Outline each blood parasite and name the species.
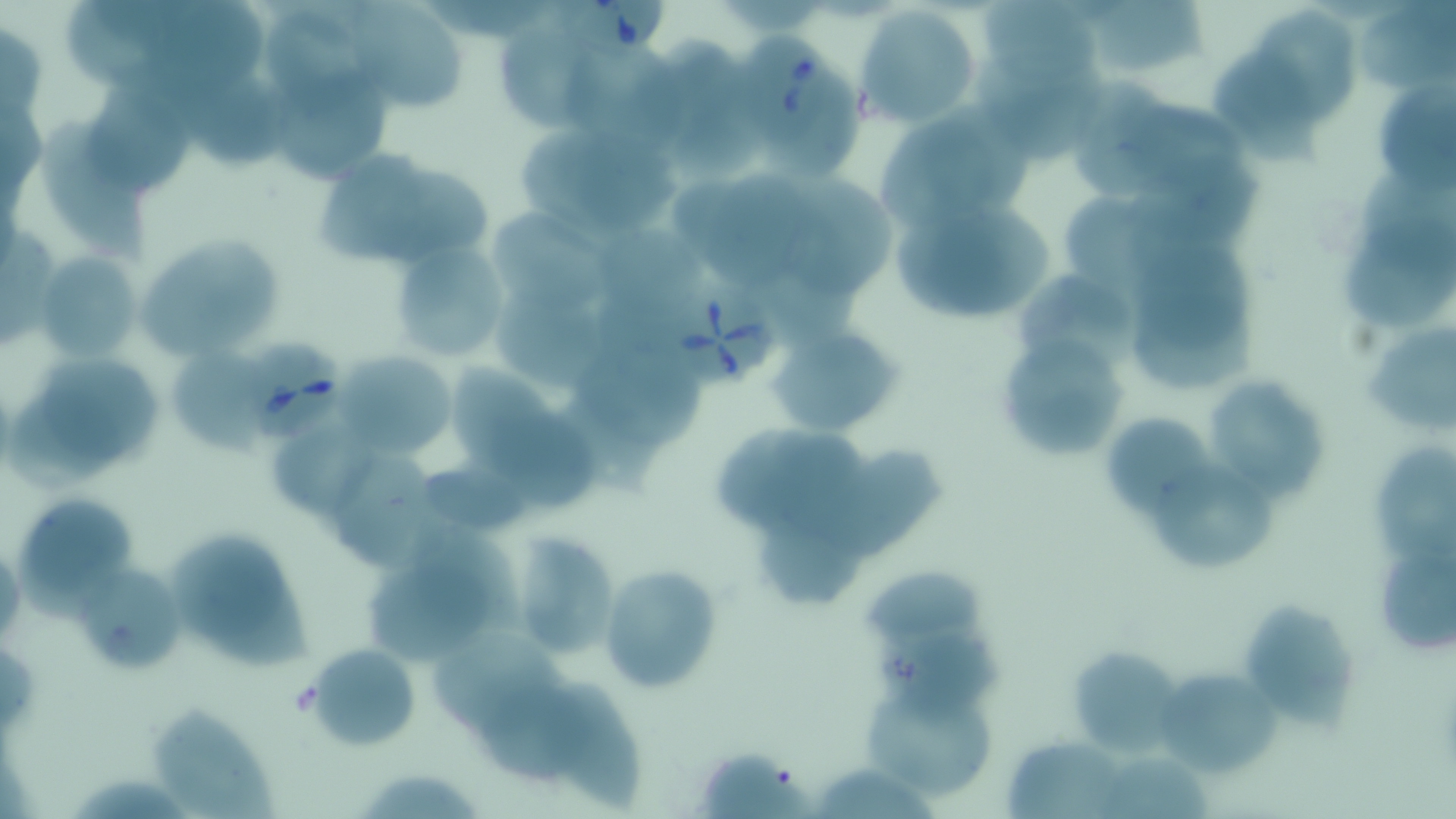

Approximate bounding boxes as named x1/y1/x2/y2 corners in pixels.
Babesia divergens-infected red blood cells: (x1=552, y1=1, x2=667, y2=58), (x1=731, y1=18, x2=832, y2=138), (x1=664, y1=282, x2=774, y2=386), (x1=235, y1=341, x2=348, y2=443).
No Plasmodium falciparum, Plasmodium ovale, Plasmodium malariae, Plasmodium vivax, or Trypanosoma brucei observed.

{
  "slide_level_diagnosis": "Babesia divergens",
  "field_of_view": "single",
  "uninfected_red_blood_cell_locations": "approximate bounding boxes as named x1/y1/x2/y2 corners in pixels: (x1=63, y1=0, x2=170, y2=87), (x1=986, y1=0, x2=1102, y2=85), (x1=1093, y1=0, x2=1212, y2=71), (x1=1358, y1=0, x2=1456, y2=96), (x1=359, y1=3, x2=467, y2=114), (x1=156, y1=4, x2=270, y2=90), (x1=856, y1=4, x2=984, y2=127), (x1=1259, y1=8, x2=1358, y2=123), (x1=262, y1=10, x2=367, y2=89), (x1=498, y1=19, x2=601, y2=127), (x1=653, y1=34, x2=745, y2=122), (x1=563, y1=37, x2=677, y2=153), (x1=978, y1=44, x2=1106, y2=166), (x1=1215, y1=49, x2=1325, y2=175), (x1=266, y1=63, x2=393, y2=183), (x1=179, y1=68, x2=288, y2=171), (x1=768, y1=71, x2=854, y2=177), (x1=1078, y1=77, x2=1175, y2=199), (x1=1374, y1=82, x2=1456, y2=201), (x1=82, y1=86, x2=195, y2=190), (x1=674, y1=98, x2=764, y2=181), (x1=1118, y1=99, x2=1249, y2=195), (x1=880, y1=115, x2=997, y2=229), (x1=41, y1=118, x2=149, y2=265), (x1=517, y1=123, x2=680, y2=249), (x1=318, y1=144, x2=421, y2=266), (x1=1141, y1=157, x2=1274, y2=241), (x1=388, y1=167, x2=502, y2=269), (x1=702, y1=171, x2=826, y2=288), (x1=793, y1=177, x2=899, y2=298), (x1=1360, y1=178, x2=1456, y2=280), (x1=894, y1=194, x2=1059, y2=328), (x1=1063, y1=197, x2=1176, y2=286), (x1=490, y1=204, x2=611, y2=320), (x1=600, y1=229, x2=714, y2=309), (x1=136, y1=234, x2=285, y2=357), (x1=1135, y1=235, x2=1253, y2=357), (x1=1341, y1=236, x2=1454, y2=322), (x1=387, y1=238, x2=512, y2=364), (x1=38, y1=252, x2=144, y2=367), (x1=757, y1=264, x2=859, y2=349), (x1=1016, y1=275, x2=1143, y2=371), (x1=595, y1=282, x2=694, y2=365), (x1=489, y1=294, x2=614, y2=386), (x1=1364, y1=318, x2=1456, y2=434), (x1=767, y1=324, x2=901, y2=438), (x1=995, y1=340, x2=1126, y2=463), (x1=583, y1=345, x2=706, y2=450), (x1=33, y1=350, x2=163, y2=465), (x1=335, y1=352, x2=456, y2=460), (x1=452, y1=359, x2=562, y2=466), (x1=1204, y1=377, x2=1327, y2=500), (x1=558, y1=388, x2=667, y2=495), (x1=1109, y1=406, x2=1208, y2=514), (x1=262, y1=408, x2=373, y2=523), (x1=490, y1=410, x2=601, y2=509), (x1=716, y1=426, x2=823, y2=526), (x1=779, y1=432, x2=875, y2=539), (x1=1362, y1=440, x2=1455, y2=553), (x1=839, y1=450, x2=945, y2=556), (x1=339, y1=456, x2=432, y2=568), (x1=1153, y1=463, x2=1282, y2=570), (x1=427, y1=468, x2=540, y2=530), (x1=13, y1=490, x2=141, y2=608), (x1=353, y1=521, x2=519, y2=665), (x1=167, y1=526, x2=309, y2=673), (x1=765, y1=529, x2=872, y2=610), (x1=508, y1=531, x2=620, y2=663), (x1=1377, y1=551, x2=1456, y2=656), (x1=597, y1=564, x2=724, y2=696), (x1=78, y1=566, x2=187, y2=674), (x1=1242, y1=596, x2=1360, y2=738), (x1=874, y1=625, x2=1009, y2=728), (x1=431, y1=639, x2=567, y2=736), (x1=306, y1=643, x2=422, y2=750), (x1=1066, y1=647, x2=1186, y2=758), (x1=1156, y1=659, x2=1286, y2=775), (x1=539, y1=675, x2=649, y2=814), (x1=480, y1=686, x2=600, y2=781), (x1=858, y1=688, x2=998, y2=800), (x1=150, y1=704, x2=280, y2=818), (x1=1004, y1=737, x2=1134, y2=819), (x1=705, y1=753, x2=816, y2=818), (x1=1106, y1=759, x2=1217, y2=819), (x1=817, y1=764, x2=947, y2=819), (x1=355, y1=765, x2=485, y2=818)",
  "stain": "May-Grünwald-Giemsa",
  "image_size": "1456×819 pixels",
  "modality": "light microscopy",
  "magnification": "1000x",
  "preparation": "thin blood smear"
}